Classify this cell by malaria status.
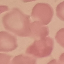
Uninfected.

Summary:
  - Preparation: thin blood smear
  - Image type: cell patch, automatically extracted from a larger field of view and resized to 64 × 64 pixels
  - Capture: smartphone camera at the microscope eyepiece
  - Stain: Giemsa